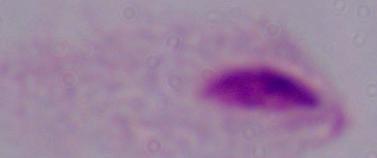

modality = photomicrograph
magnification = 1000x
identification = trichomonad